Locate and identify every blood parasite.
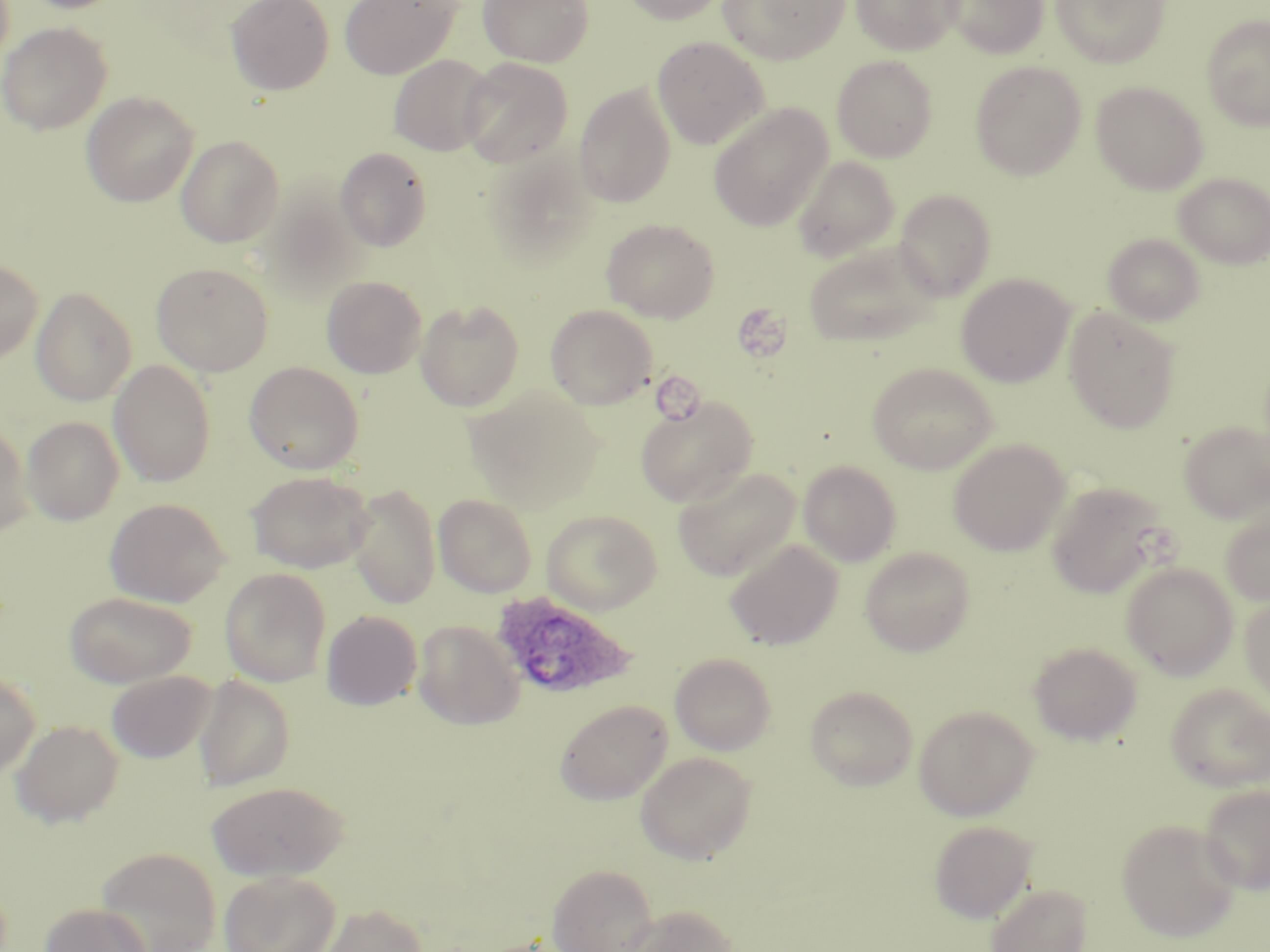
Approximate bounding boxes as [x1, y1, x2, y2] in pixels.
Plasmodium ovale-infected red blood cells: [490, 591, 638, 702].
No Plasmodium falciparum, Plasmodium malariae, Plasmodium vivax, Babesia divergens, or Trypanosoma brucei observed.

Summary:
  - Platelet locations: [739, 304, 790, 364], [652, 373, 709, 427]
  - Uninfected red blood cell locations: [18, 0, 130, 13], [226, 0, 334, 95], [340, 0, 461, 80], [478, 0, 594, 67], [619, 0, 731, 25], [718, 0, 850, 64], [850, 0, 962, 56], [941, 0, 1050, 58], [1051, 0, 1170, 67], [1201, 15, 1270, 130], [0, 22, 112, 135], [652, 37, 769, 149], [389, 55, 495, 156], [832, 55, 938, 162], [459, 58, 573, 168], [970, 61, 1087, 181], [1091, 80, 1209, 194], [574, 83, 676, 208], [81, 92, 199, 207], [709, 103, 833, 232], [176, 135, 284, 247], [335, 147, 432, 251], [792, 156, 900, 263], [1173, 172, 1270, 269], [893, 188, 997, 300], [258, 191, 366, 301], [601, 218, 720, 322], [1103, 233, 1205, 326], [803, 239, 940, 348], [0, 258, 43, 365], [151, 262, 274, 376], [956, 273, 1075, 387], [322, 276, 427, 378], [31, 286, 137, 406], [415, 299, 524, 411], [546, 304, 657, 409], [1064, 308, 1181, 433], [108, 360, 216, 487], [244, 361, 364, 474], [867, 362, 998, 474], [466, 386, 606, 515], [635, 395, 758, 508], [22, 416, 124, 525], [1179, 420, 1270, 523], [0, 422, 32, 538], [948, 439, 1070, 556], [798, 460, 901, 566], [673, 467, 800, 582], [246, 470, 375, 573], [1046, 481, 1171, 598], [346, 483, 441, 609], [434, 494, 537, 597], [104, 498, 231, 607], [542, 509, 663, 614], [1220, 510, 1270, 606], [724, 538, 843, 651], [860, 546, 976, 656], [1120, 562, 1239, 680], [220, 568, 331, 687], [65, 591, 197, 688], [1240, 595, 1270, 707], [321, 610, 422, 710], [413, 620, 524, 729], [1028, 641, 1142, 746], [670, 653, 777, 755], [0, 670, 40, 780], [106, 670, 216, 763], [194, 675, 296, 791], [1166, 684, 1270, 791], [805, 685, 918, 790], [555, 699, 672, 805], [913, 704, 1039, 820], [11, 720, 123, 827], [635, 752, 757, 864], [207, 780, 349, 880], [1198, 783, 1270, 895], [1117, 819, 1240, 942], [928, 820, 1038, 923], [95, 847, 221, 952], [546, 864, 658, 952], [219, 870, 340, 952], [985, 883, 1093, 952], [39, 902, 153, 952], [317, 903, 428, 952], [621, 904, 739, 952]
  - Slide-level diagnosis: Plasmodium ovale
  - Preparation: thin blood film
  - Field of view: one of a larger specimen
  - Stain: May-Grünwald-Giemsa
  - Image size: 1270×952 pixels
  - Magnification: 1000x
  - Modality: light microscopy